Assess for malaria.
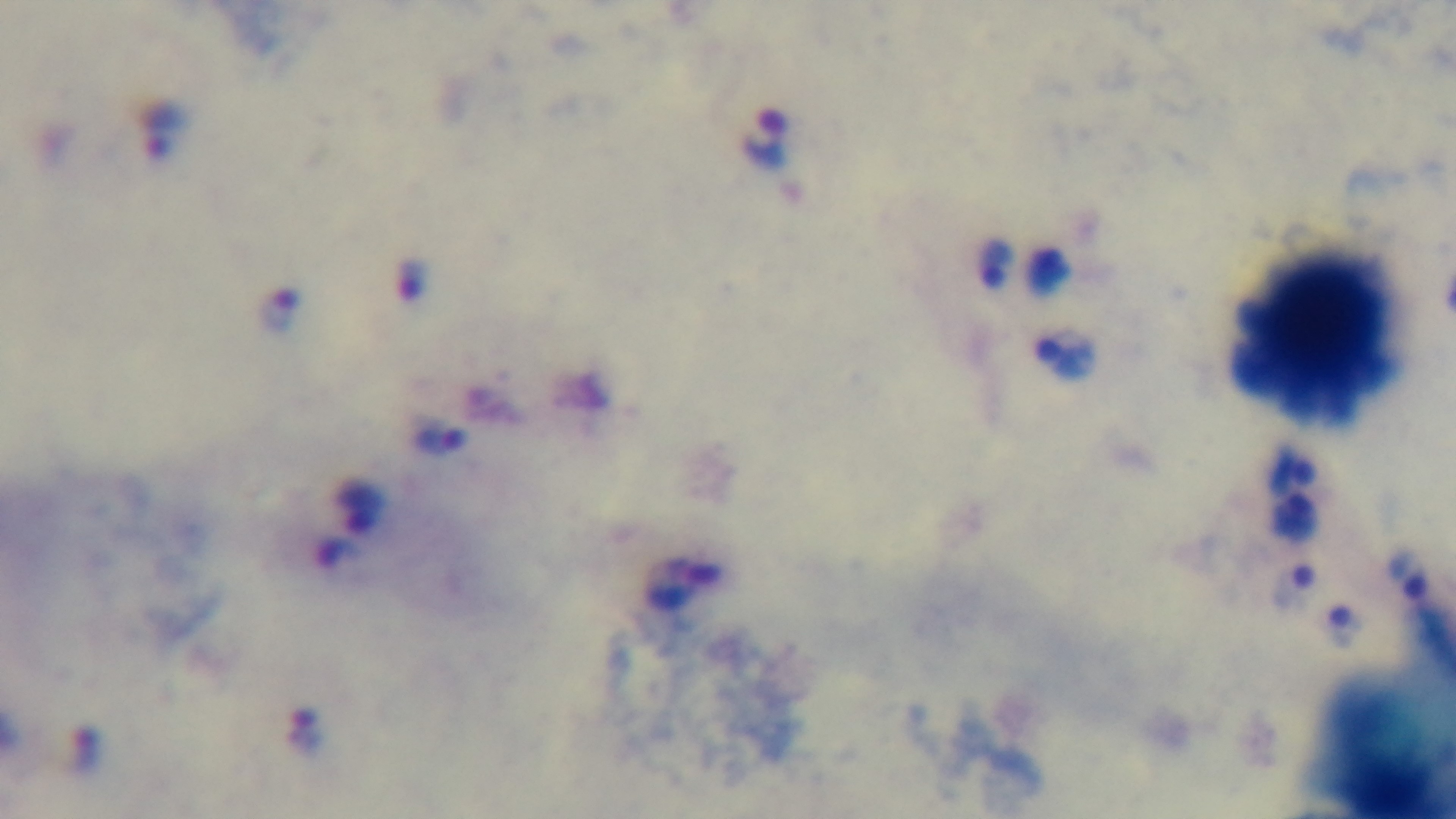
Positive.

field of view = single
preparation = thick blood film
objective = 100x oil immersion
stain = Giemsa
capture = mounted 4K digital camera
modality = light microscopy